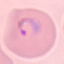

Summary:
  - Malaria status: parasitized
  - Stain: Giemsa
  - Preparation: thin smear
  - Image type: cell patch, automatically extracted from a larger field of view and resized to 64 × 64 pixels
  - Capture: smartphone through the microscope eyepiece